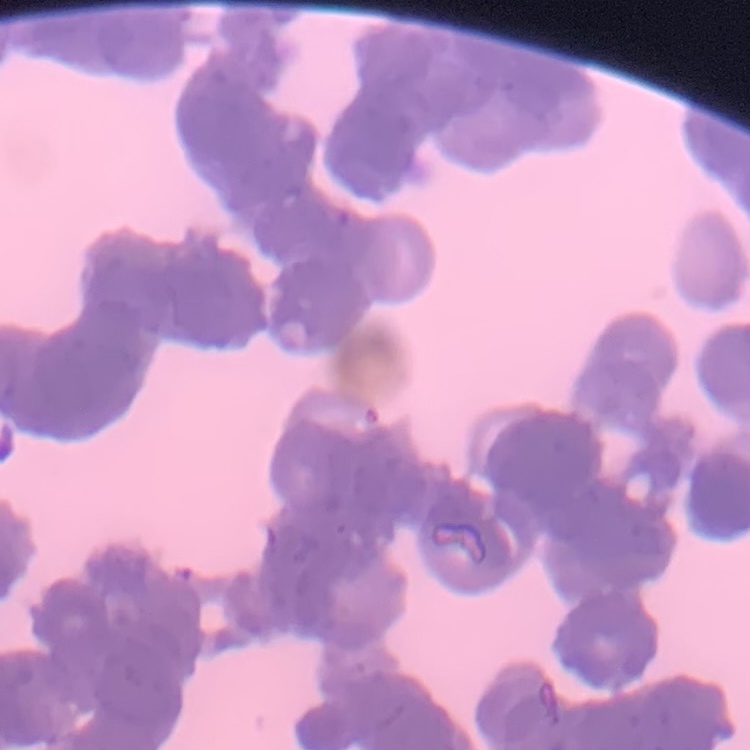

{
  "red_blood_cell_morphology": "rouleaux formation",
  "image_type": "one tile cut from a larger photomicrograph",
  "preparation": "thin peripheral smear",
  "stain": "Field's or Giemsa"
}